Locate every Plasmodium parasite.
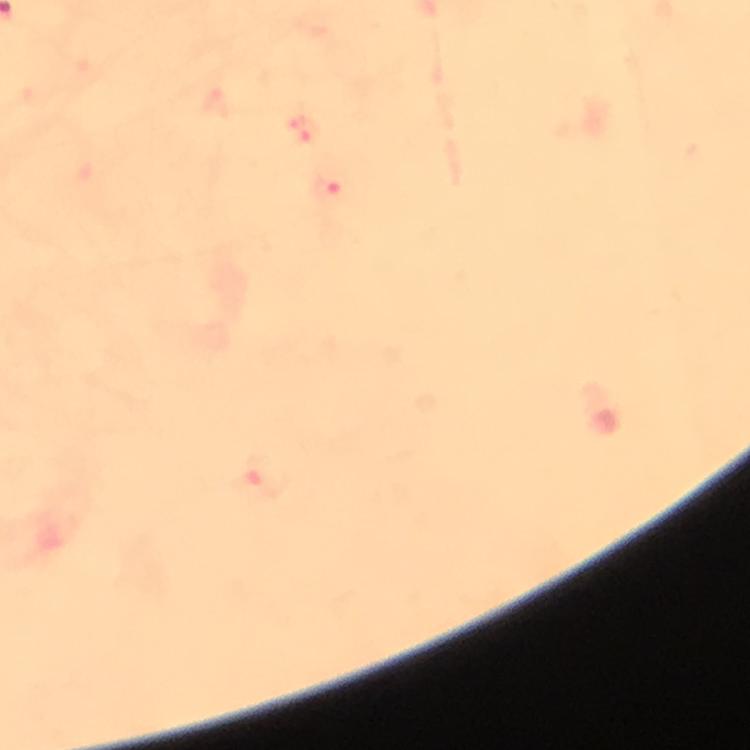
Approximate centers as (x, y) in pixels.
Plasmodium parasites: (329, 186), (268, 476).

Summary:
  - Cropped from: one field of view
  - Capture: smartphone mounted on the microscope
  - Magnification: 100x
  - Image size: 750×750 pixels
  - Stain: Giemsa
  - Immersion oil: applied
  - Context: from a diagnostic examination for malaria
  - Preparation: thick smear